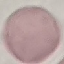

Result: negative for malaria parasites. Cell patch, automatically extracted from a larger field of view and resized to 64 × 64 pixels. Giemsa-stained preparation. Acquired by smartphone through the microscope eyepiece. Thin blood smear.